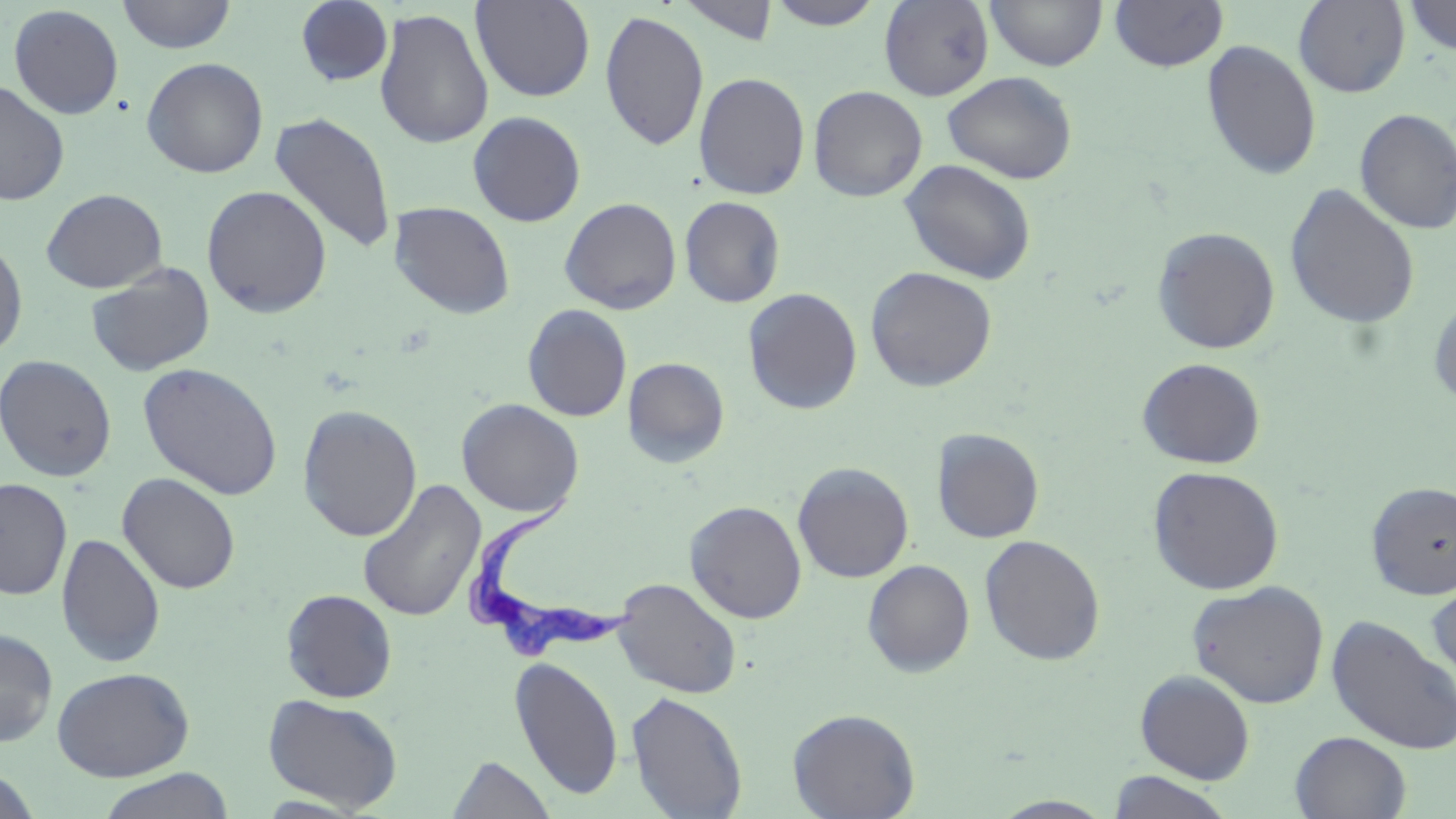
slide_level_diagnosis: Trypanosoma brucei
preparation: thin blood smear
modality: optical microscopy
trypanosoma_brucei_locations: 'approximate bounding boxes as [x1, y1, x2, y2] in pixels: [464, 497, 637, 665]'
field_of_view: one of a larger specimen
magnification: 1000x
uninfected_red_blood_cell_locations: 'approximate bounding boxes as [x1, y1, x2, y2] in pixels: [116, 0, 237, 54], [295, 0, 394, 87], [471, 0, 596, 103], [677, 0, 780, 45], [764, 0, 886, 29], [879, 0, 994, 101], [985, 0, 1107, 71], [1109, 0, 1229, 73], [1401, 0, 1456, 56], [1293, 1, 1410, 97], [8, 4, 124, 120], [374, 8, 494, 149], [599, 9, 709, 152], [1201, 39, 1322, 181], [141, 57, 268, 178], [693, 71, 810, 200], [942, 71, 1079, 184], [0, 79, 70, 205], [808, 85, 928, 202], [1354, 107, 1456, 235], [269, 111, 397, 255], [467, 111, 587, 227], [899, 159, 1037, 284], [1283, 183, 1420, 330], [201, 184, 333, 318], [41, 188, 168, 293], [679, 196, 785, 307], [559, 197, 682, 314], [389, 201, 516, 319], [1151, 225, 1281, 355], [0, 238, 28, 362], [86, 262, 215, 377], [865, 266, 998, 392], [742, 288, 863, 415], [1428, 294, 1456, 412], [522, 304, 633, 422], [0, 354, 117, 482], [623, 357, 729, 467], [1136, 357, 1266, 469], [137, 362, 284, 500], [457, 399, 584, 517], [297, 405, 422, 542], [932, 428, 1044, 543], [792, 462, 914, 583], [1147, 465, 1284, 595], [117, 472, 240, 594], [0, 478, 73, 601], [357, 480, 486, 623], [1365, 480, 1456, 600], [684, 500, 807, 624], [56, 533, 166, 668], [979, 533, 1106, 665], [863, 557, 1105, 670], [862, 559, 975, 676], [613, 577, 742, 699], [1426, 578, 1456, 693], [1187, 580, 1329, 709], [281, 589, 398, 703], [1326, 614, 1456, 756], [0, 628, 58, 747], [510, 655, 624, 801], [53, 666, 194, 781], [1135, 669, 1256, 783], [626, 690, 748, 819], [263, 693, 403, 813], [787, 708, 920, 819], [1290, 731, 1411, 818], [447, 754, 557, 819], [0, 767, 43, 818], [96, 769, 235, 819], [1107, 771, 1234, 818], [991, 796, 1116, 818]'
image_size: 1456×819 pixels
stain: May-Grünwald-Giemsa